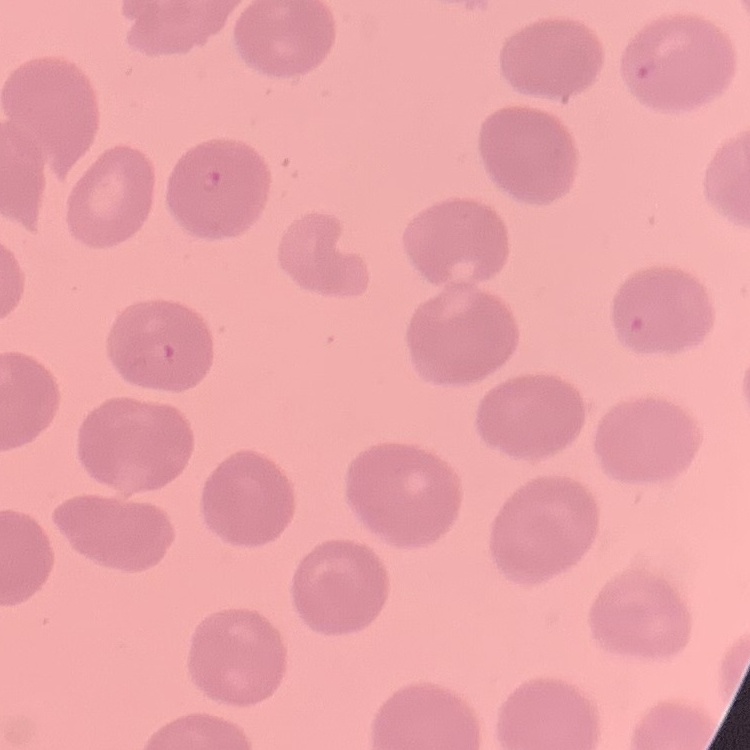

erythrocyte morphology = no rouleaux formation
stain = Field's or Giemsa
image type = square crop of a larger photomicrograph
preparation = thin peripheral smear